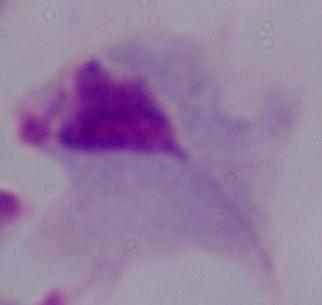 A trichomonad is seen. 1000x magnification. Photomicrograph.